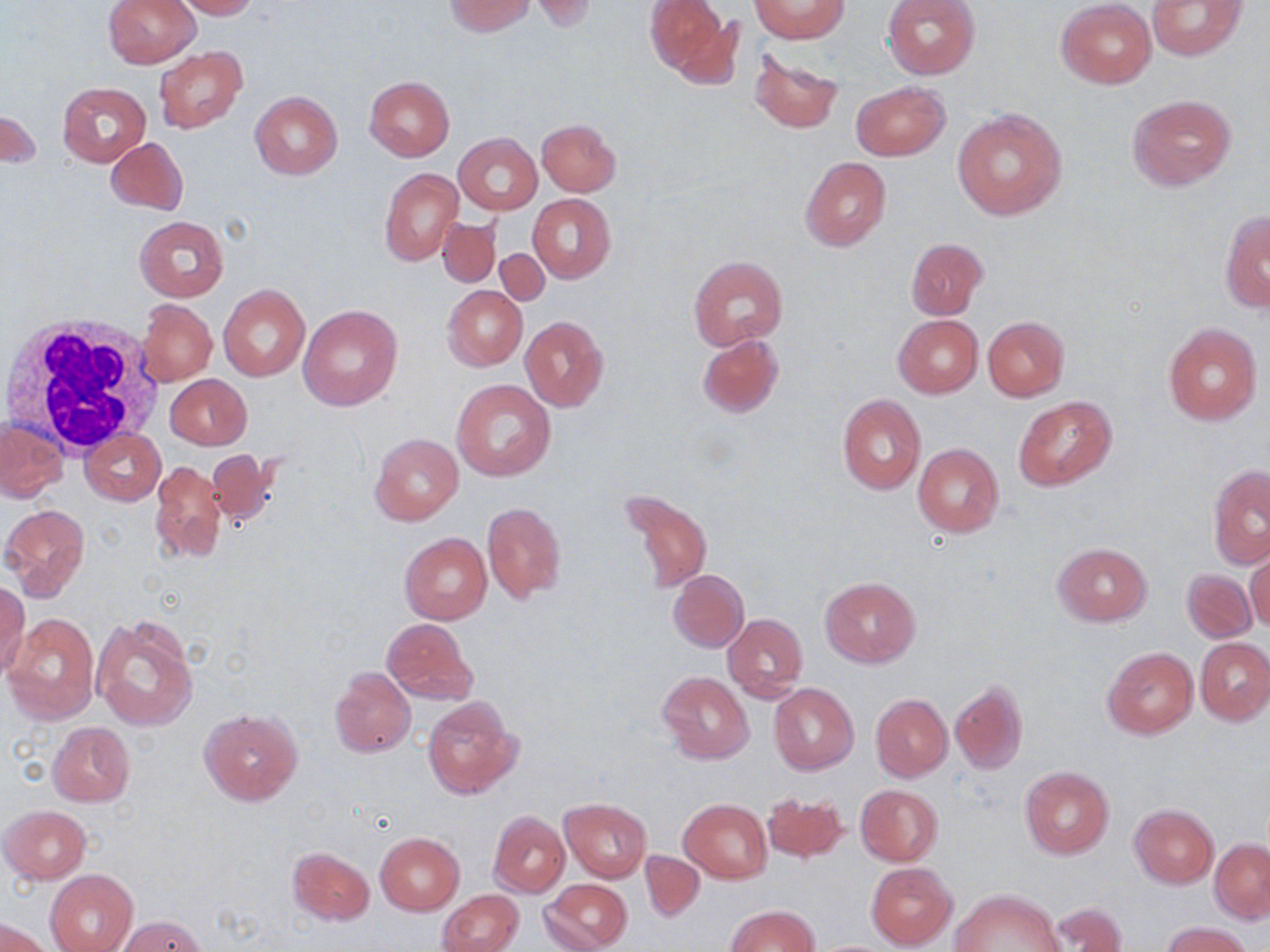
slide-level diagnosis = negative for blood parasites
stain = May-Grünwald-Giemsa
preparation = thin blood film
uninfected red blood cell locations = approximate bounding boxes as named x1/y1/x2/y2 corners in pixels: (x1=103, y1=0, x2=201, y2=69), (x1=172, y1=0, x2=260, y2=19), (x1=444, y1=0, x2=536, y2=36), (x1=530, y1=0, x2=597, y2=31), (x1=645, y1=0, x2=736, y2=83), (x1=752, y1=0, x2=848, y2=41), (x1=882, y1=0, x2=979, y2=80), (x1=1056, y1=0, x2=1155, y2=88), (x1=1146, y1=0, x2=1246, y2=61), (x1=153, y1=47, x2=247, y2=134), (x1=751, y1=53, x2=843, y2=133), (x1=364, y1=77, x2=454, y2=160), (x1=57, y1=81, x2=151, y2=166), (x1=851, y1=81, x2=950, y2=161), (x1=249, y1=90, x2=342, y2=180), (x1=1127, y1=94, x2=1237, y2=189), (x1=1, y1=106, x2=39, y2=173), (x1=951, y1=108, x2=1068, y2=221), (x1=537, y1=118, x2=620, y2=196), (x1=453, y1=133, x2=542, y2=215), (x1=106, y1=137, x2=187, y2=215), (x1=800, y1=157, x2=891, y2=251), (x1=379, y1=168, x2=462, y2=265), (x1=528, y1=194, x2=615, y2=282), (x1=1220, y1=211, x2=1270, y2=313), (x1=134, y1=215, x2=229, y2=301), (x1=437, y1=216, x2=501, y2=287), (x1=905, y1=237, x2=988, y2=320), (x1=495, y1=247, x2=549, y2=304), (x1=689, y1=255, x2=788, y2=351), (x1=442, y1=285, x2=528, y2=370), (x1=219, y1=286, x2=310, y2=381), (x1=140, y1=299, x2=217, y2=385), (x1=299, y1=303, x2=403, y2=412), (x1=893, y1=314, x2=983, y2=398), (x1=519, y1=315, x2=609, y2=412), (x1=982, y1=315, x2=1070, y2=401), (x1=1162, y1=322, x2=1263, y2=425), (x1=697, y1=334, x2=783, y2=418), (x1=167, y1=374, x2=252, y2=448), (x1=451, y1=380, x2=556, y2=482), (x1=837, y1=394, x2=927, y2=496), (x1=1014, y1=396, x2=1118, y2=490), (x1=0, y1=417, x2=68, y2=501), (x1=81, y1=429, x2=165, y2=505), (x1=370, y1=432, x2=464, y2=525), (x1=912, y1=444, x2=1004, y2=537), (x1=206, y1=447, x2=282, y2=528), (x1=150, y1=459, x2=226, y2=565), (x1=1209, y1=464, x2=1270, y2=569), (x1=618, y1=487, x2=714, y2=595), (x1=481, y1=501, x2=566, y2=603), (x1=3, y1=504, x2=90, y2=597), (x1=400, y1=532, x2=492, y2=625), (x1=1052, y1=542, x2=1152, y2=626), (x1=1246, y1=550, x2=1270, y2=635), (x1=1181, y1=567, x2=1256, y2=642), (x1=668, y1=569, x2=748, y2=652), (x1=819, y1=577, x2=920, y2=667), (x1=0, y1=581, x2=31, y2=679), (x1=5, y1=612, x2=99, y2=725), (x1=723, y1=612, x2=807, y2=702), (x1=91, y1=614, x2=199, y2=732), (x1=381, y1=618, x2=478, y2=705), (x1=1195, y1=637, x2=1270, y2=725), (x1=1102, y1=647, x2=1199, y2=739), (x1=329, y1=667, x2=416, y2=758), (x1=657, y1=672, x2=753, y2=763), (x1=950, y1=681, x2=1027, y2=774), (x1=768, y1=682, x2=858, y2=774), (x1=870, y1=693, x2=952, y2=781), (x1=422, y1=696, x2=522, y2=799), (x1=199, y1=709, x2=302, y2=805), (x1=48, y1=722, x2=136, y2=806), (x1=1019, y1=767, x2=1114, y2=859), (x1=856, y1=783, x2=944, y2=866), (x1=762, y1=791, x2=849, y2=862), (x1=560, y1=798, x2=651, y2=882), (x1=680, y1=798, x2=772, y2=882), (x1=1129, y1=804, x2=1218, y2=888), (x1=0, y1=805, x2=90, y2=883), (x1=488, y1=810, x2=570, y2=898), (x1=374, y1=833, x2=464, y2=916), (x1=1210, y1=839, x2=1269, y2=922), (x1=286, y1=847, x2=375, y2=925), (x1=639, y1=851, x2=705, y2=922), (x1=866, y1=861, x2=957, y2=950), (x1=45, y1=869, x2=138, y2=952), (x1=542, y1=878, x2=631, y2=951), (x1=952, y1=888, x2=1064, y2=952), (x1=439, y1=889, x2=523, y2=952), (x1=1044, y1=902, x2=1127, y2=952), (x1=726, y1=905, x2=819, y2=951), (x1=117, y1=916, x2=209, y2=951), (x1=3, y1=917, x2=55, y2=951), (x1=1162, y1=921, x2=1253, y2=952)
magnification = 1000x
white blood cell locations = approximate bounding boxes as named x1/y1/x2/y2 corners in pixels: (x1=5, y1=313, x2=170, y2=455)
field of view = single
modality = optical microscopy
image size = 1270×952 pixels